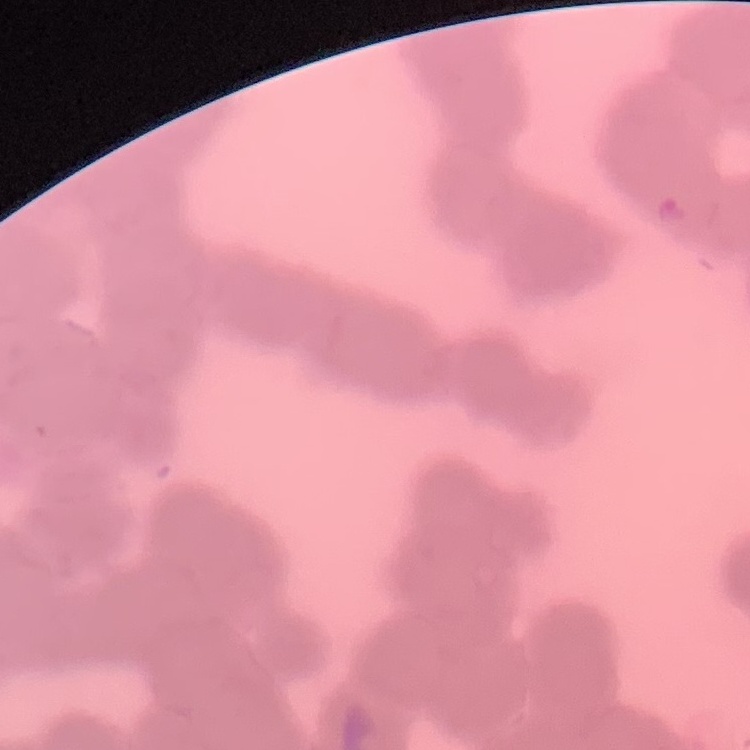 The red blood cells show rouleaux formation. One tile cut from a larger photomicrograph. Field's or Giemsa stain. Thin blood smear.